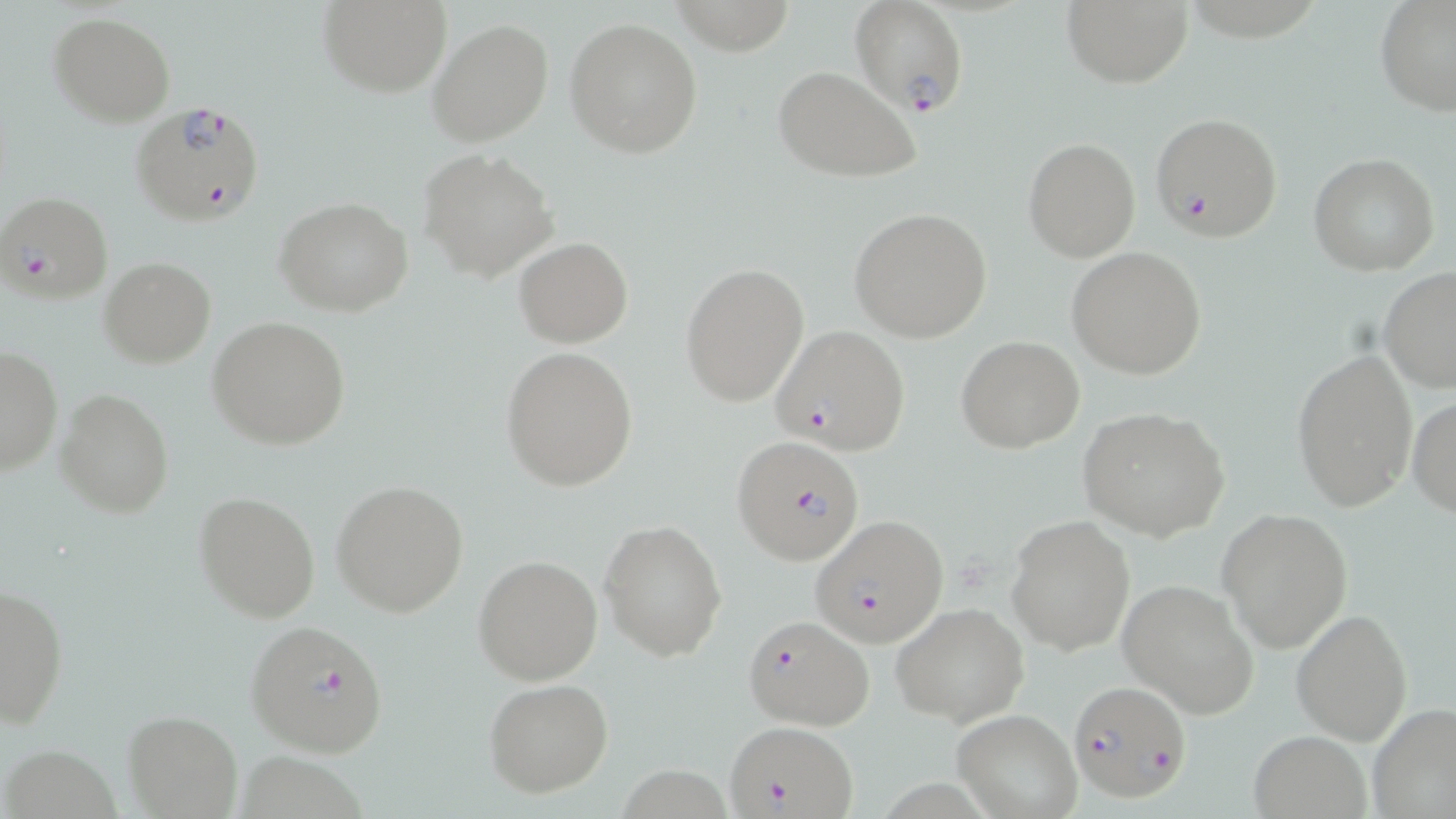
Summary:
  - Coordinate format: approximate bounding boxes as [x1, y1, x2, y2] in pixels
  - Plasmodium falciparum-infected red blood cell locations: [849, 1, 970, 117], [131, 100, 266, 228], [1152, 111, 1283, 241], [2, 192, 114, 305], [770, 326, 912, 455], [731, 436, 866, 566], [815, 515, 949, 647], [744, 615, 875, 735], [245, 619, 389, 756], [1068, 679, 1191, 804], [726, 721, 855, 818]
  - Uninfected red blood cell locations: [316, 0, 451, 96], [670, 0, 799, 55], [1058, 0, 1194, 89], [1375, 1, 1456, 117], [49, 13, 174, 125], [427, 17, 554, 147], [564, 17, 703, 158], [772, 65, 924, 184], [1023, 138, 1141, 260], [420, 147, 559, 283], [1308, 154, 1441, 275], [276, 199, 414, 317], [848, 207, 992, 342], [513, 236, 632, 348], [1066, 248, 1207, 379], [99, 255, 215, 367], [680, 263, 810, 406], [1379, 267, 1456, 393], [209, 316, 350, 450], [955, 336, 1084, 453], [0, 346, 62, 476], [500, 347, 638, 491], [1291, 349, 1417, 513], [56, 390, 173, 518], [1407, 396, 1456, 519], [1078, 407, 1231, 541], [331, 480, 470, 617], [194, 491, 319, 621], [1217, 507, 1354, 652], [1005, 514, 1135, 656], [600, 518, 728, 660], [473, 555, 604, 685], [1118, 579, 1260, 719], [1, 583, 70, 730], [891, 602, 1029, 727], [1291, 608, 1414, 745], [483, 678, 614, 799], [1367, 702, 1456, 819], [953, 709, 1082, 818], [123, 710, 242, 819], [1248, 730, 1372, 819]
  - Slide-level diagnosis: Plasmodium falciparum
  - Stain: May-Grünwald-Giemsa
  - Field of view: single
  - Modality: optical microscopy
  - Magnification: 1000x
  - Preparation: thin blood film
  - Image size: 1456×819 pixels